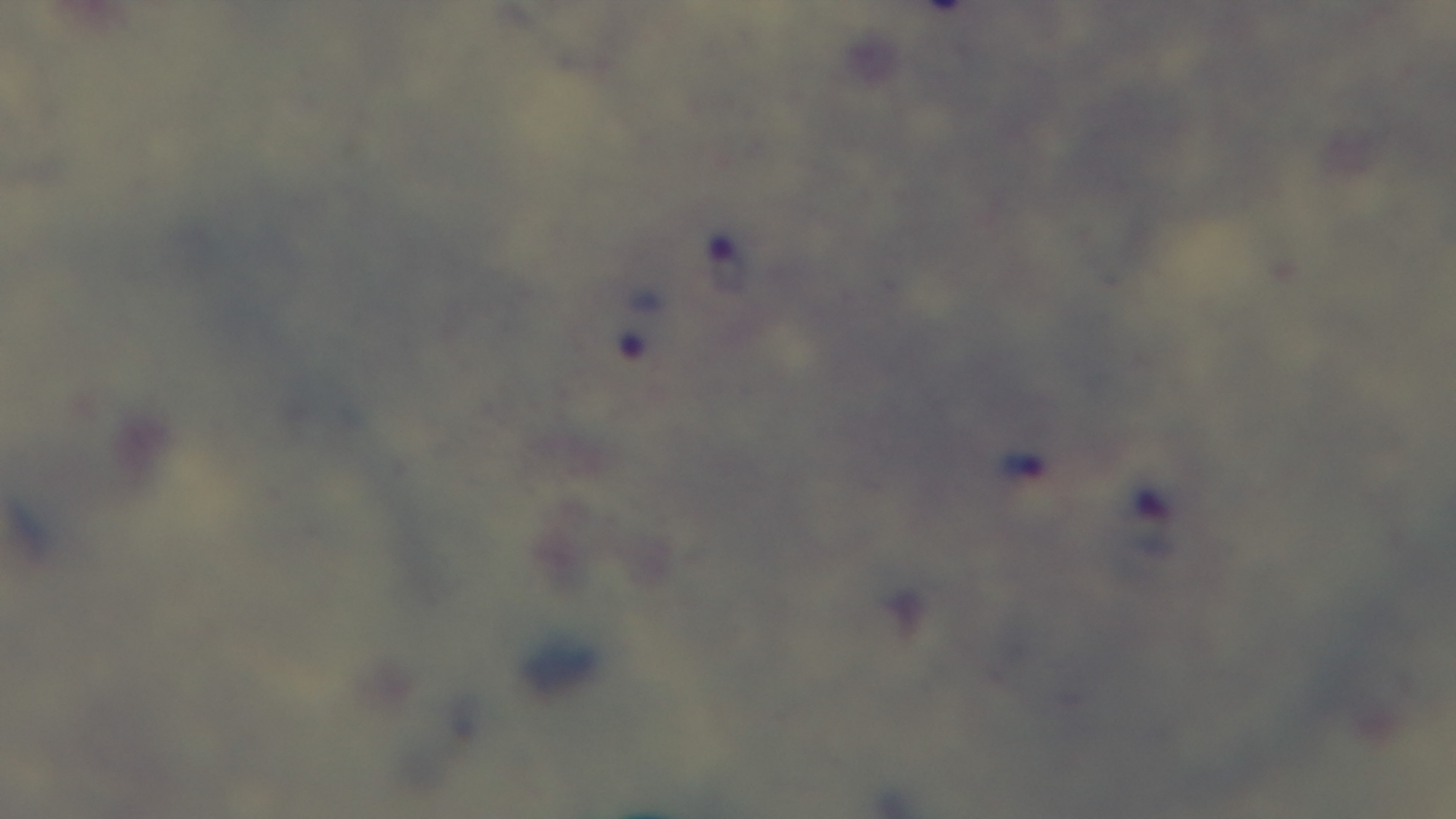
Photomicrograph. Mounted 4K digital camera. Malaria status: positive. Preparation: thick blood film. Single field of view. Giemsa stain. 100x oil-immersion objective.